Outline each Plasmodium falciparum-infected red blood cell.
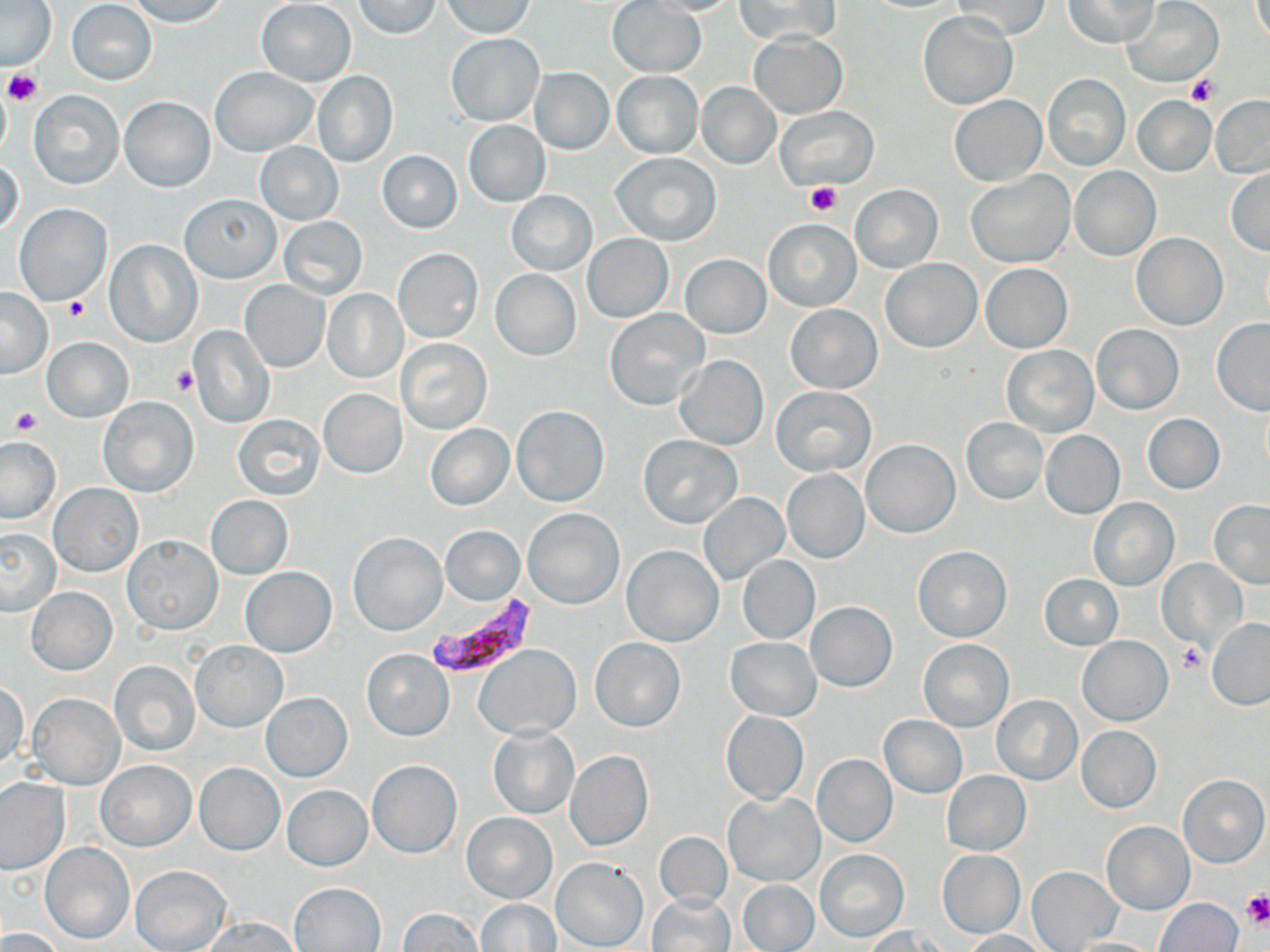
Approximate bounding boxes as [x1, y1, x2, y2] in pixels.
Plasmodium falciparum-infected red blood cells: [424, 592, 541, 680].

Summary:
  - Platelet locations: [3, 69, 44, 105], [1185, 74, 1220, 109], [804, 183, 841, 216], [62, 295, 89, 321], [170, 366, 197, 395], [10, 408, 42, 434], [1177, 644, 1206, 673], [1242, 892, 1270, 928]
  - Uninfected red blood cell locations: [125, 0, 233, 27], [444, 0, 537, 37], [445, 0, 538, 84], [640, 0, 744, 15], [734, 0, 840, 45], [1063, 0, 1161, 47], [0, 1, 57, 70], [67, 1, 157, 85], [256, 1, 357, 86], [353, 1, 443, 39], [607, 1, 705, 77], [953, 1, 1051, 39], [1123, 2, 1223, 88], [917, 12, 1017, 109], [749, 31, 847, 119], [446, 33, 543, 126], [528, 67, 614, 155], [210, 68, 318, 156], [312, 71, 398, 167], [611, 71, 704, 157], [1043, 74, 1130, 170], [696, 83, 781, 169], [27, 90, 124, 188], [949, 95, 1047, 187], [1210, 95, 1270, 177], [119, 96, 215, 192], [1131, 97, 1216, 178], [776, 106, 878, 189], [463, 119, 551, 207], [255, 141, 344, 226], [375, 150, 463, 233], [610, 152, 722, 246], [0, 157, 25, 238], [1070, 165, 1160, 262], [1225, 168, 1270, 255], [966, 169, 1075, 267], [851, 184, 942, 273], [506, 189, 597, 277], [179, 192, 281, 282], [14, 203, 112, 306], [277, 215, 367, 301], [764, 219, 861, 311], [582, 233, 673, 322], [1132, 233, 1228, 330], [105, 240, 203, 347], [393, 247, 483, 343], [680, 253, 771, 339], [881, 259, 982, 352], [982, 263, 1072, 352], [489, 269, 581, 360], [240, 280, 330, 373], [0, 287, 53, 379], [323, 288, 409, 383], [784, 304, 883, 393], [605, 309, 708, 410], [1211, 319, 1270, 415], [1091, 325, 1185, 414], [190, 326, 273, 428], [41, 336, 134, 423], [395, 338, 492, 435], [1002, 345, 1098, 438], [673, 355, 768, 450], [770, 386, 876, 476], [318, 388, 406, 478], [98, 396, 198, 497], [511, 404, 609, 507], [1142, 413, 1226, 495], [233, 414, 325, 501], [961, 418, 1048, 504], [425, 423, 514, 510], [1039, 429, 1126, 518], [638, 434, 743, 529], [0, 435, 64, 524], [862, 439, 961, 537], [782, 469, 870, 565], [49, 483, 144, 576], [698, 494, 789, 584], [204, 495, 293, 579], [1089, 497, 1179, 590], [1208, 499, 1270, 588], [523, 508, 624, 609], [438, 525, 525, 605], [0, 529, 62, 616], [348, 531, 447, 635], [124, 535, 222, 636], [622, 544, 723, 646], [914, 545, 1011, 641], [737, 555, 820, 644], [1157, 559, 1248, 651], [241, 567, 336, 658], [1039, 573, 1124, 651], [26, 588, 116, 675], [805, 601, 899, 692], [1207, 618, 1270, 708], [1078, 636, 1172, 726], [725, 637, 821, 720], [591, 638, 685, 732], [919, 639, 1014, 732], [192, 640, 287, 732], [474, 644, 582, 740], [361, 649, 455, 741], [108, 659, 200, 757], [1, 680, 29, 770], [25, 692, 125, 789], [261, 692, 351, 781], [992, 695, 1082, 785], [721, 711, 809, 804], [879, 714, 968, 799], [1075, 725, 1162, 812], [488, 726, 580, 820], [564, 749, 653, 852], [811, 754, 897, 848], [366, 760, 462, 858], [97, 761, 195, 851], [194, 763, 285, 856], [941, 770, 1030, 855], [1179, 774, 1269, 867], [0, 777, 69, 875], [283, 785, 372, 871], [723, 792, 824, 886], [461, 812, 558, 905], [1101, 820, 1193, 915], [654, 832, 733, 910], [39, 842, 136, 944], [816, 848, 908, 943], [937, 849, 1025, 938], [550, 856, 649, 952], [131, 865, 233, 952], [1026, 867, 1121, 950], [739, 880, 819, 951], [288, 881, 386, 951], [647, 894, 735, 952], [475, 899, 562, 950], [1156, 899, 1242, 952], [396, 907, 484, 951], [202, 916, 300, 952], [862, 926, 946, 951], [0, 927, 67, 952], [962, 929, 1054, 951], [1066, 937, 1161, 952]
  - Slide-level diagnosis: Plasmodium falciparum
  - Preparation: thin blood film
  - Field of view: one of a larger specimen
  - Modality: light microscopy
  - Stain: May-Grünwald-Giemsa
  - Image size: 1270×952 pixels
  - Magnification: 1000x